Identify the blood parasite species.
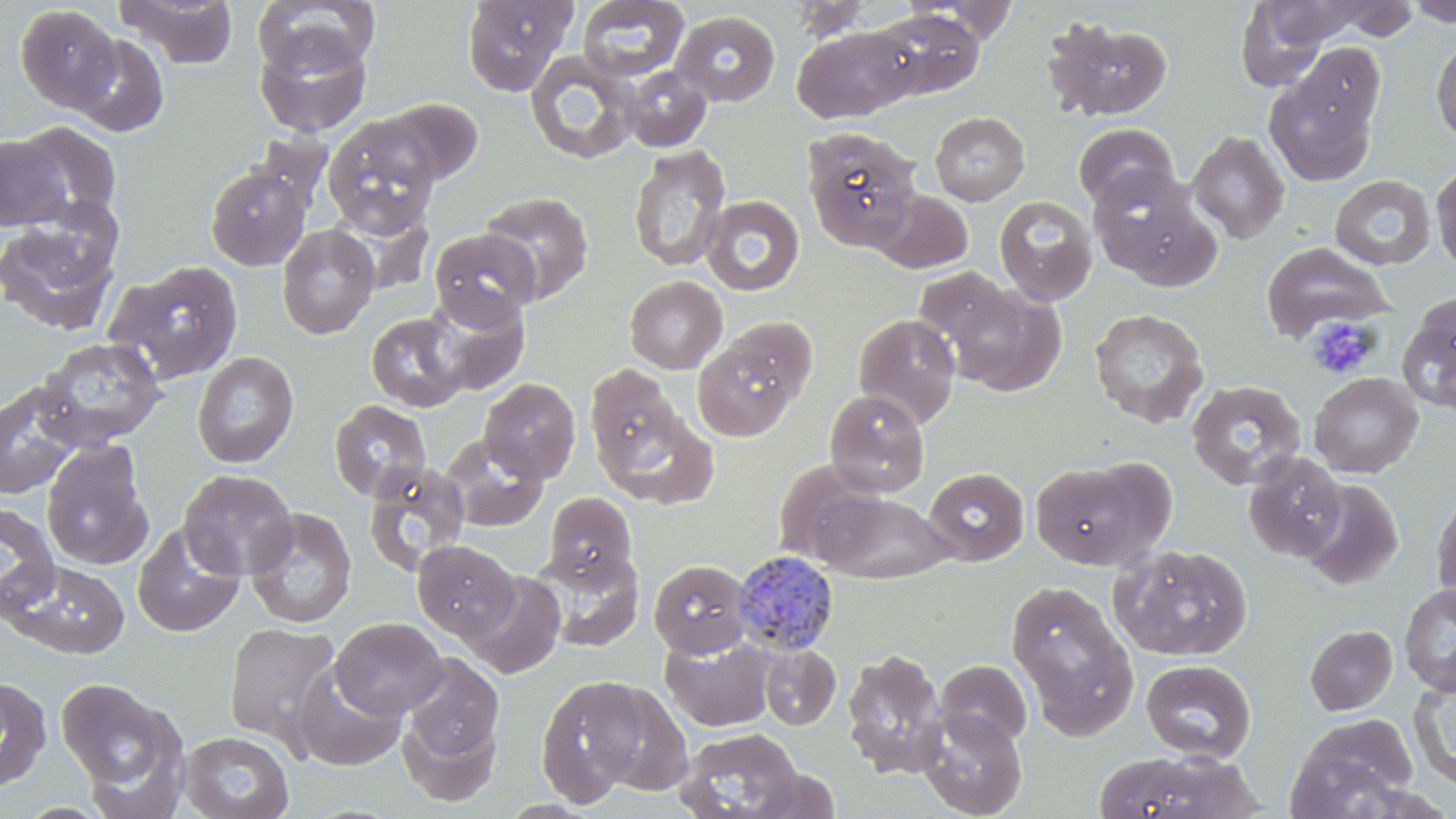
Plasmodium malariae.

Summary:
  - Coordinate format: approximate bounding boxes as named x1/y1/x2/y2 corners in pixels
  - Platelet locations: (x1=1306, y1=315, x2=1380, y2=379)
  - Plasmodium malariae-infected red blood cell locations: (x1=733, y1=551, x2=840, y2=656)
  - Uninfected red blood cell locations: (x1=115, y1=0, x2=241, y2=69), (x1=460, y1=0, x2=577, y2=95), (x1=577, y1=0, x2=689, y2=82), (x1=786, y1=0, x2=877, y2=41), (x1=908, y1=0, x2=1023, y2=44), (x1=1404, y1=0, x2=1456, y2=27), (x1=253, y1=1, x2=380, y2=77), (x1=1235, y1=1, x2=1331, y2=89), (x1=1260, y1=1, x2=1380, y2=48), (x1=1311, y1=1, x2=1425, y2=43), (x1=15, y1=5, x2=122, y2=112), (x1=871, y1=9, x2=985, y2=101), (x1=670, y1=10, x2=781, y2=106), (x1=1043, y1=16, x2=1174, y2=122), (x1=791, y1=24, x2=918, y2=123), (x1=254, y1=30, x2=372, y2=136), (x1=69, y1=34, x2=170, y2=137), (x1=1431, y1=38, x2=1456, y2=142), (x1=1293, y1=44, x2=1384, y2=141), (x1=524, y1=50, x2=642, y2=165), (x1=621, y1=66, x2=713, y2=152), (x1=1264, y1=66, x2=1381, y2=186), (x1=379, y1=97, x2=484, y2=186), (x1=930, y1=111, x2=1029, y2=205), (x1=323, y1=117, x2=442, y2=238), (x1=16, y1=121, x2=122, y2=224), (x1=1073, y1=122, x2=1179, y2=211), (x1=802, y1=126, x2=923, y2=250), (x1=1186, y1=130, x2=1290, y2=244), (x1=1, y1=135, x2=72, y2=231), (x1=628, y1=145, x2=731, y2=272), (x1=1431, y1=162, x2=1456, y2=276), (x1=205, y1=165, x2=311, y2=270), (x1=1086, y1=165, x2=1212, y2=284), (x1=1330, y1=175, x2=1436, y2=271), (x1=869, y1=189, x2=973, y2=274), (x1=479, y1=191, x2=594, y2=304), (x1=701, y1=195, x2=805, y2=297), (x1=993, y1=195, x2=1098, y2=305), (x1=0, y1=213, x2=123, y2=335), (x1=276, y1=223, x2=379, y2=339), (x1=429, y1=229, x2=541, y2=328), (x1=1260, y1=242, x2=1392, y2=344), (x1=105, y1=260, x2=245, y2=385), (x1=624, y1=275, x2=727, y2=374), (x1=941, y1=280, x2=1068, y2=396), (x1=428, y1=292, x2=530, y2=395), (x1=1397, y1=292, x2=1456, y2=416), (x1=1089, y1=308, x2=1209, y2=428), (x1=366, y1=312, x2=467, y2=411), (x1=853, y1=313, x2=961, y2=428), (x1=720, y1=316, x2=820, y2=407), (x1=692, y1=335, x2=803, y2=442), (x1=35, y1=336, x2=168, y2=449), (x1=191, y1=351, x2=299, y2=468), (x1=585, y1=366, x2=681, y2=471), (x1=1308, y1=372, x2=1422, y2=478), (x1=479, y1=378, x2=581, y2=483), (x1=0, y1=379, x2=87, y2=499), (x1=1186, y1=379, x2=1307, y2=490), (x1=824, y1=389, x2=930, y2=498), (x1=329, y1=399, x2=432, y2=502), (x1=601, y1=409, x2=719, y2=508), (x1=440, y1=434, x2=549, y2=531), (x1=41, y1=440, x2=153, y2=570), (x1=1242, y1=451, x2=1347, y2=563), (x1=1030, y1=461, x2=1156, y2=569), (x1=364, y1=463, x2=471, y2=575), (x1=923, y1=467, x2=1029, y2=565), (x1=178, y1=469, x2=298, y2=580), (x1=1299, y1=480, x2=1403, y2=591), (x1=1431, y1=485, x2=1456, y2=609), (x1=809, y1=487, x2=956, y2=583), (x1=543, y1=491, x2=637, y2=585), (x1=0, y1=501, x2=61, y2=619), (x1=244, y1=507, x2=356, y2=629), (x1=132, y1=522, x2=244, y2=637), (x1=413, y1=540, x2=519, y2=641), (x1=1109, y1=543, x2=1253, y2=661), (x1=534, y1=547, x2=645, y2=651), (x1=648, y1=558, x2=752, y2=658), (x1=3, y1=559, x2=130, y2=659), (x1=462, y1=571, x2=566, y2=679), (x1=1005, y1=579, x2=1137, y2=735), (x1=1399, y1=584, x2=1456, y2=696), (x1=331, y1=617, x2=447, y2=719), (x1=223, y1=621, x2=342, y2=753), (x1=1305, y1=624, x2=1398, y2=715), (x1=661, y1=635, x2=774, y2=731), (x1=759, y1=644, x2=841, y2=730), (x1=841, y1=648, x2=948, y2=779), (x1=401, y1=655, x2=504, y2=766), (x1=1140, y1=659, x2=1257, y2=762), (x1=935, y1=660, x2=1033, y2=750), (x1=292, y1=664, x2=407, y2=772), (x1=536, y1=675, x2=652, y2=805), (x1=0, y1=676, x2=52, y2=793), (x1=55, y1=676, x2=184, y2=809), (x1=1409, y1=677, x2=1456, y2=793), (x1=398, y1=705, x2=502, y2=807), (x1=917, y1=708, x2=1027, y2=818), (x1=1285, y1=715, x2=1419, y2=818), (x1=673, y1=726, x2=805, y2=819), (x1=180, y1=730, x2=295, y2=819), (x1=1092, y1=751, x2=1250, y2=819)
  - Image size: 1456×819 pixels
  - Preparation: thin blood film
  - Field of view: one of a larger specimen
  - Stain: May-Grünwald-Giemsa
  - Modality: light microscopy
  - Magnification: 1000x